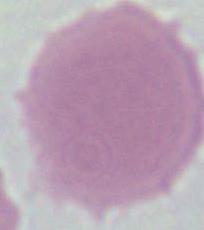

1000x magnification. A red blood cell is shown. Micrograph.